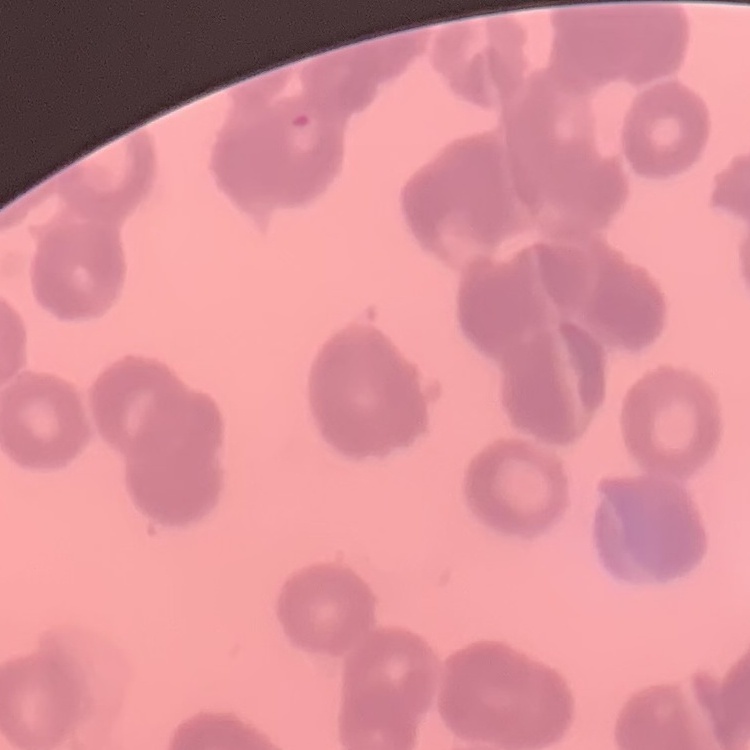

red blood cell morphology = rouleaux formation
preparation = thin blood film
image type = square crop of a larger photomicrograph
stain = Field's or Giemsa